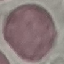
Summary:
  - Malaria status: uninfected
  - Preparation: thin blood film
  - Stain: Giemsa
  - Image type: automatically extracted cell patch, resized to 64 × 64 pixels
  - Capture: smartphone camera at the microscope eyepiece